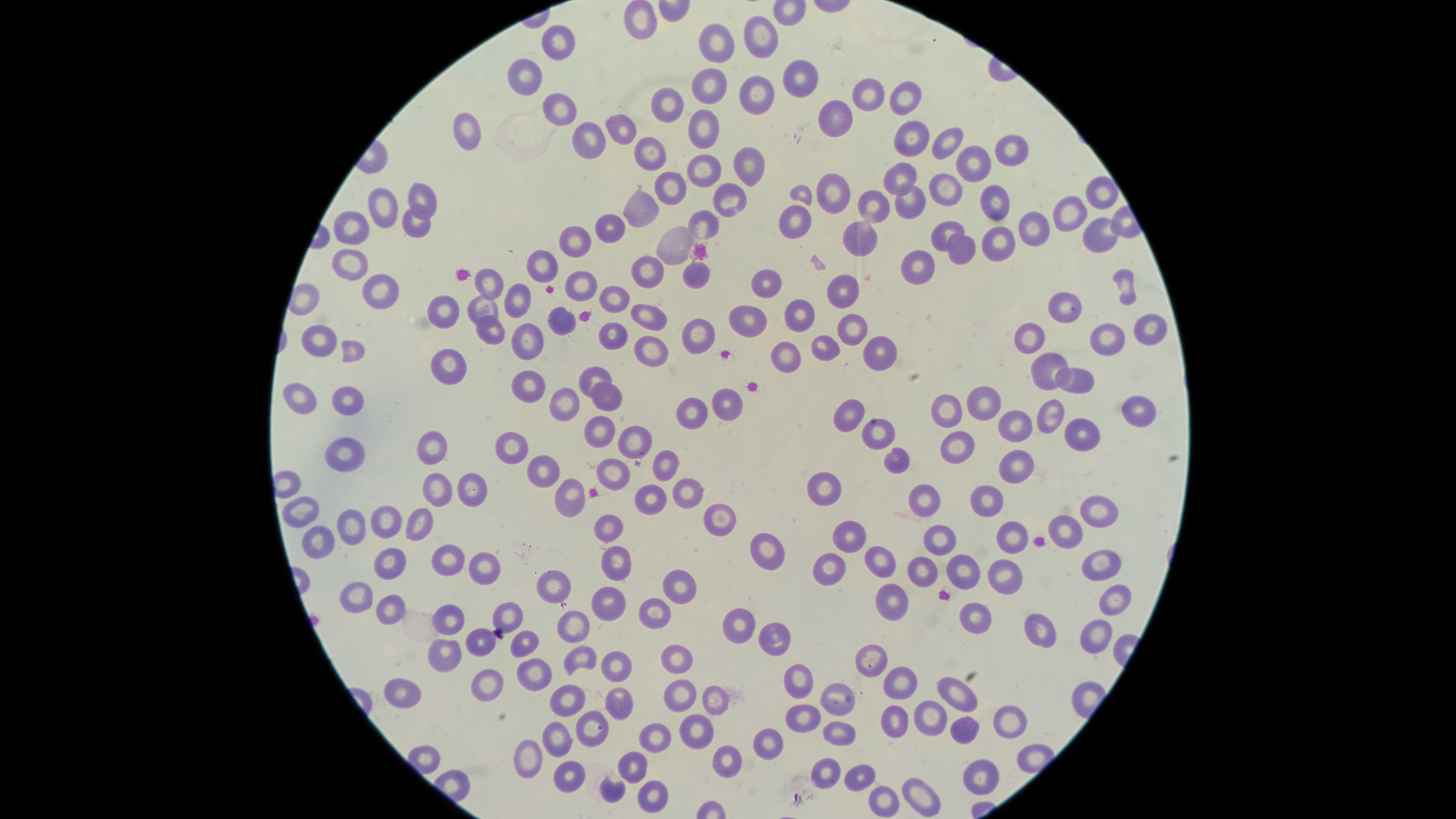

Approximate marker points as [x, y] in pixels.
Summary:
  - Uninfected red blood cells: [643, 23], [760, 35], [713, 40], [557, 41], [531, 73], [799, 80], [700, 90], [865, 94], [756, 95], [905, 97], [559, 105], [668, 105], [833, 120], [621, 125], [702, 130], [469, 134], [912, 138], [591, 139], [943, 142], [1010, 147], [650, 156], [747, 164], [975, 164], [700, 171], [901, 177], [670, 187], [946, 188], [831, 193], [1099, 193], [729, 197], [997, 197], [424, 199], [876, 203], [908, 203], [642, 209], [384, 212], [1072, 213], [420, 218], [703, 222], [789, 225], [605, 227], [1032, 228], [362, 231], [944, 231], [1097, 231], [866, 238], [576, 240], [999, 241], [672, 247], [957, 247], [918, 264], [353, 270], [544, 270], [643, 271], [695, 272], [767, 282], [585, 283], [382, 286], [493, 286], [847, 291], [518, 299], [614, 301], [1066, 305], [485, 310], [798, 310], [445, 312], [648, 319], [745, 319], [851, 326], [556, 327], [1146, 329], [613, 333], [1106, 334], [490, 335], [324, 337], [697, 337], [1029, 337], [531, 342], [824, 345], [645, 347], [875, 352], [351, 353], [780, 355], [1047, 365], [447, 369], [592, 374], [1079, 381], [528, 385], [605, 393], [307, 399], [343, 400], [984, 401], [726, 402], [1138, 402], [566, 404], [950, 410], [688, 413], [849, 413], [1050, 413], [1013, 428], [879, 430], [598, 432], [1080, 437], [636, 443], [964, 444], [510, 445], [433, 446], [345, 452], [899, 461], [666, 464], [1019, 467], [543, 469], [612, 469], [827, 487], [440, 489], [472, 490], [692, 493], [923, 495], [574, 496], [650, 496], [987, 500], [1094, 505], [307, 510], [385, 517], [720, 519], [421, 521], [356, 522], [608, 528], [1069, 530], [850, 533], [940, 538], [1009, 540], [319, 542], [769, 550], [1096, 560], [445, 561], [613, 561], [922, 561], [880, 562], [394, 564], [481, 565], [828, 565], [967, 568], [1000, 574], [558, 584], [682, 589], [360, 590], [890, 596], [1115, 596], [605, 602], [388, 603], [659, 608], [511, 611], [977, 611], [451, 618], [743, 621], [576, 625], [1097, 633], [1042, 634], [775, 636], [524, 638], [480, 639], [450, 653], [581, 656], [675, 656], [875, 660], [617, 664], [536, 673], [496, 678], [797, 678], [905, 680], [682, 690], [959, 692], [408, 694], [568, 696], [620, 701], [842, 702], [715, 704], [803, 709], [933, 717], [1013, 721], [895, 723], [597, 727], [698, 727], [964, 727], [841, 731], [660, 734], [764, 737], [559, 740], [527, 752], [726, 756], [636, 765], [984, 771], [823, 773], [864, 773], [570, 777], [920, 785], [619, 789], [654, 791], [883, 800]
  - Image size: 1456×819 pixels
  - Presence: no malaria parasites detected
  - Stain: Giemsa
  - Field of view: single
  - Capture: smartphone photograph through the microscope eyepiece
  - Visible region: circular
  - Preparation: thin blood smear